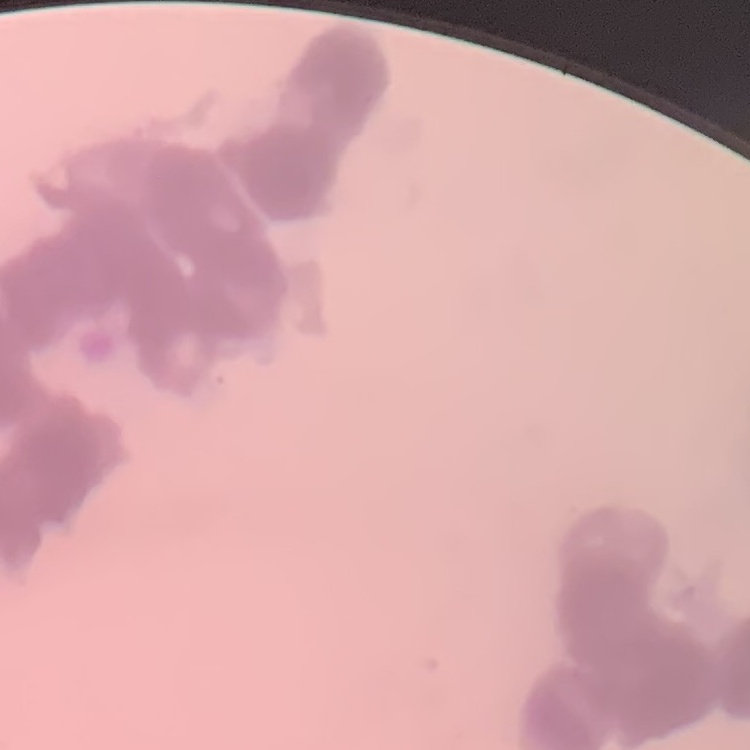

red blood cell morphology = rouleaux formation
image type = one tile cut from a larger photomicrograph
stain = Field's or Giemsa
preparation = thin peripheral smear